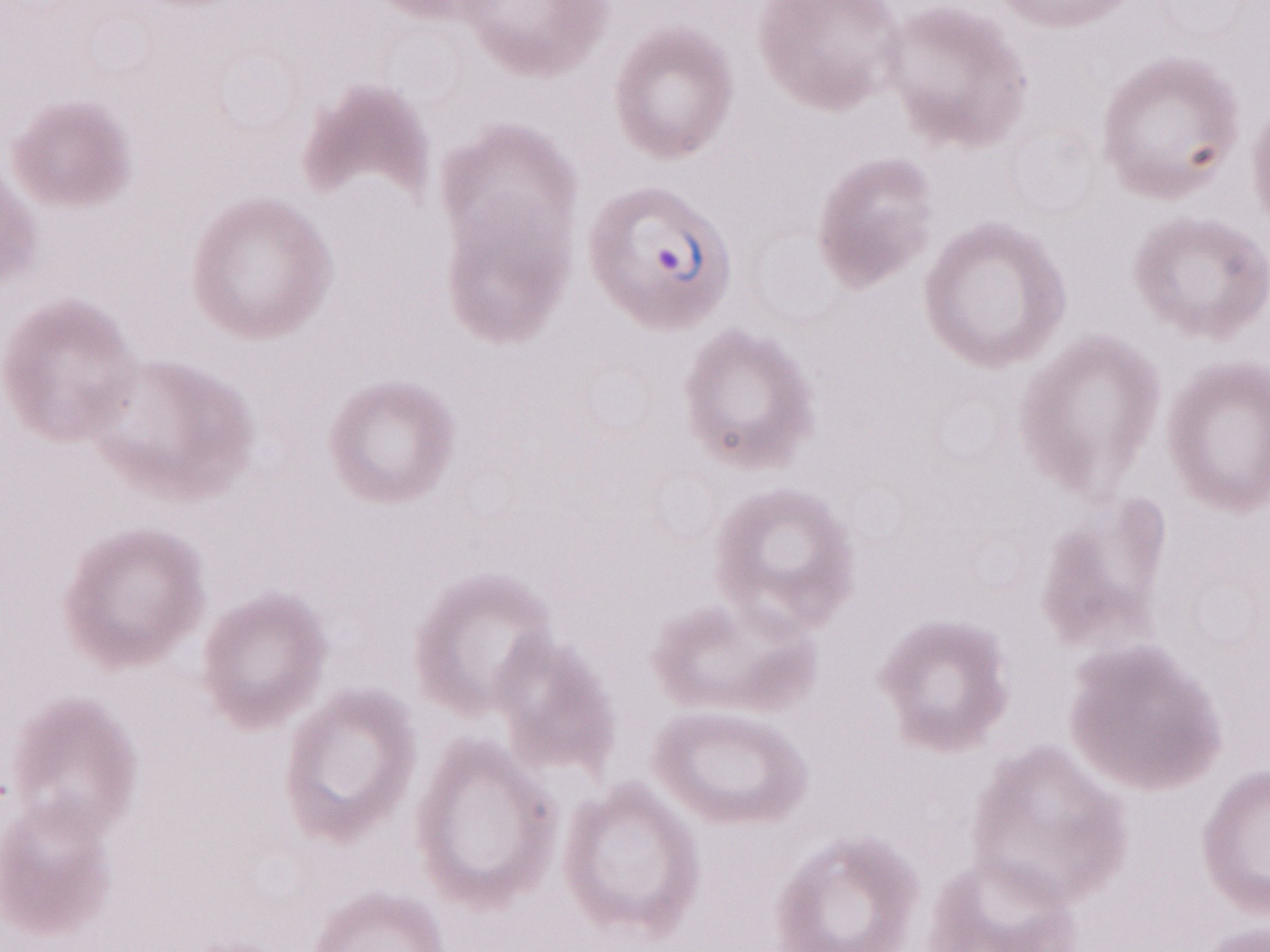

Single field of view. Patient diagnosis: malaria infection. Olympus BX43 microscope and DP73 digital camera. May-Grünwald-Giemsa (MGG) stain. Thin peripheral-blood smear. 1,000x magnification. Image is 1270×952 pixels.